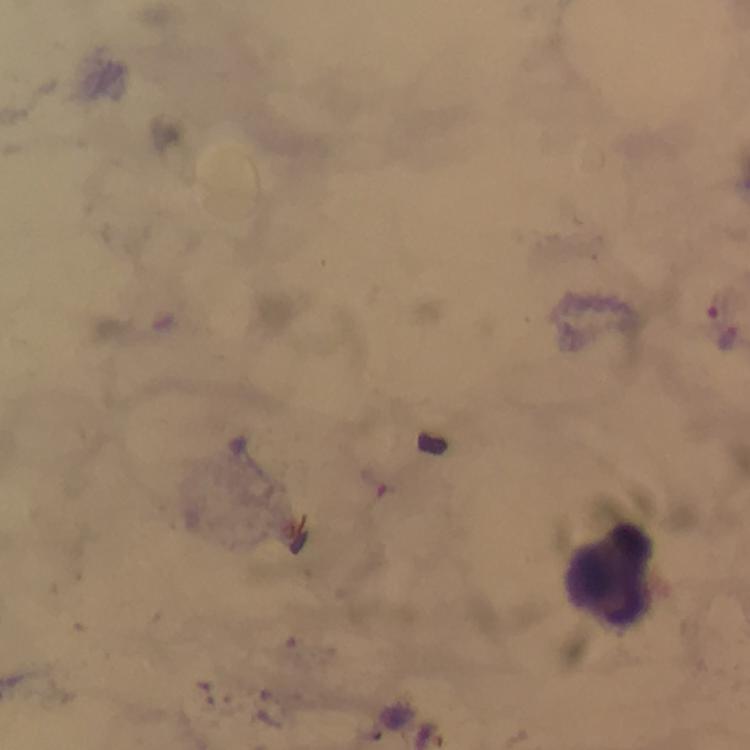

context = from a diagnostic examination for malaria
Plasmodium parasite locations = approximate centers as [x, y] in pixels: [729, 338]
image size = 750×750 pixels
preparation = thick blood film
cropped from = a single field of view
magnification = 100x
leukocyte locations = approximate centers as [x, y] in pixels: [608, 580]
stain = Giemsa
capture = smartphone mounted on the microscope
immersion oil = applied